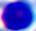
Summary:
  - Identification: leukocyte
  - Modality: photomicrograph
  - Magnification: 400x